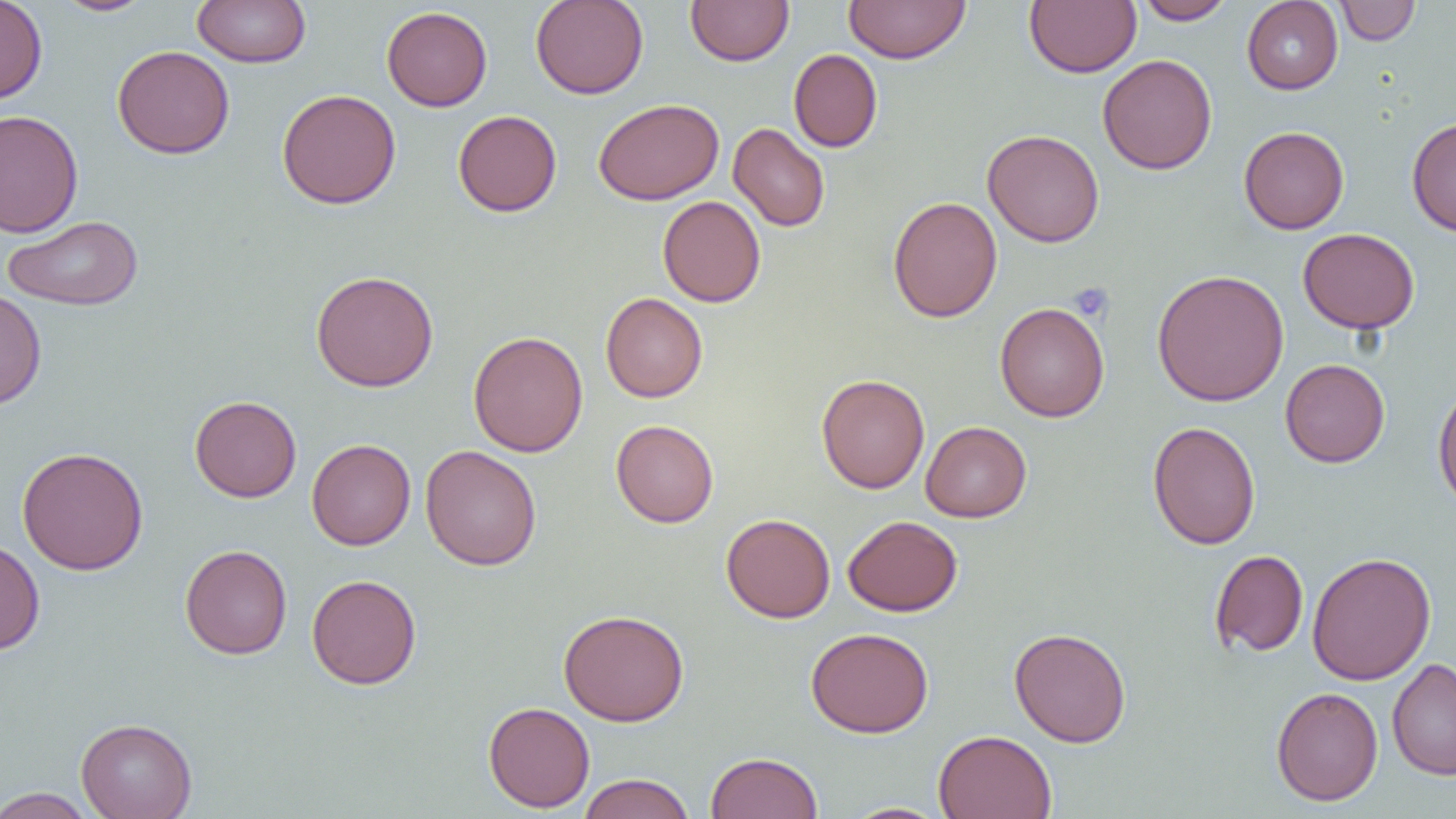

slide-level diagnosis = negative for blood parasites
magnification = 1000x
image size = 1456×819 pixels
preparation = thin blood film
platelet locations = approximate bounding boxes as (x1,y1)-(x2,y2) corner pairs in pixels: (1068,283)-(1114,322)
modality = light microscopy
field of view = one of a larger specimen
uninfected red blood cell locations = approximate bounding boxes as (x1,y1)-(x2,y2) corner pairs in pixels: (0,0)-(48,105), (52,0)-(157,16), (192,0)-(311,67), (530,0)-(648,100), (685,0)-(795,66), (844,0)-(970,64), (1024,0)-(1141,78), (1134,0)-(1236,24), (1241,0)-(1343,94), (1334,0)-(1420,45), (381,6)-(493,111), (112,45)-(235,159), (789,48)-(883,152), (1098,54)-(1217,174), (277,88)-(402,209), (594,98)-(724,205), (0,110)-(84,237), (453,110)-(562,217), (1407,116)-(1456,236), (728,122)-(830,232), (1238,126)-(1350,234), (982,129)-(1105,248), (657,195)-(766,307), (888,195)-(1002,323), (3,215)-(143,311), (1298,228)-(1420,333), (1151,268)-(1290,406), (310,270)-(439,392), (0,287)-(47,411), (601,292)-(708,402), (995,302)-(1109,422), (468,330)-(588,457), (1280,359)-(1390,467), (815,373)-(929,494), (1432,381)-(1456,511), (189,396)-(301,502), (611,420)-(719,527), (920,421)-(1032,522), (1148,421)-(1261,550), (307,438)-(416,550), (420,445)-(542,571), (16,446)-(149,575), (721,513)-(836,623), (843,515)-(962,616), (0,539)-(45,655), (180,544)-(292,659), (1209,549)-(1309,657), (1306,551)-(1436,686), (306,574)-(422,689), (558,609)-(689,726), (806,627)-(934,737), (1009,627)-(1131,747), (1387,658)-(1456,780), (1271,686)-(1383,805), (483,701)-(595,812), (76,717)-(197,819), (933,729)-(1057,819), (705,751)-(823,819), (577,773)-(695,819), (1,787)-(99,818), (840,802)-(953,819)